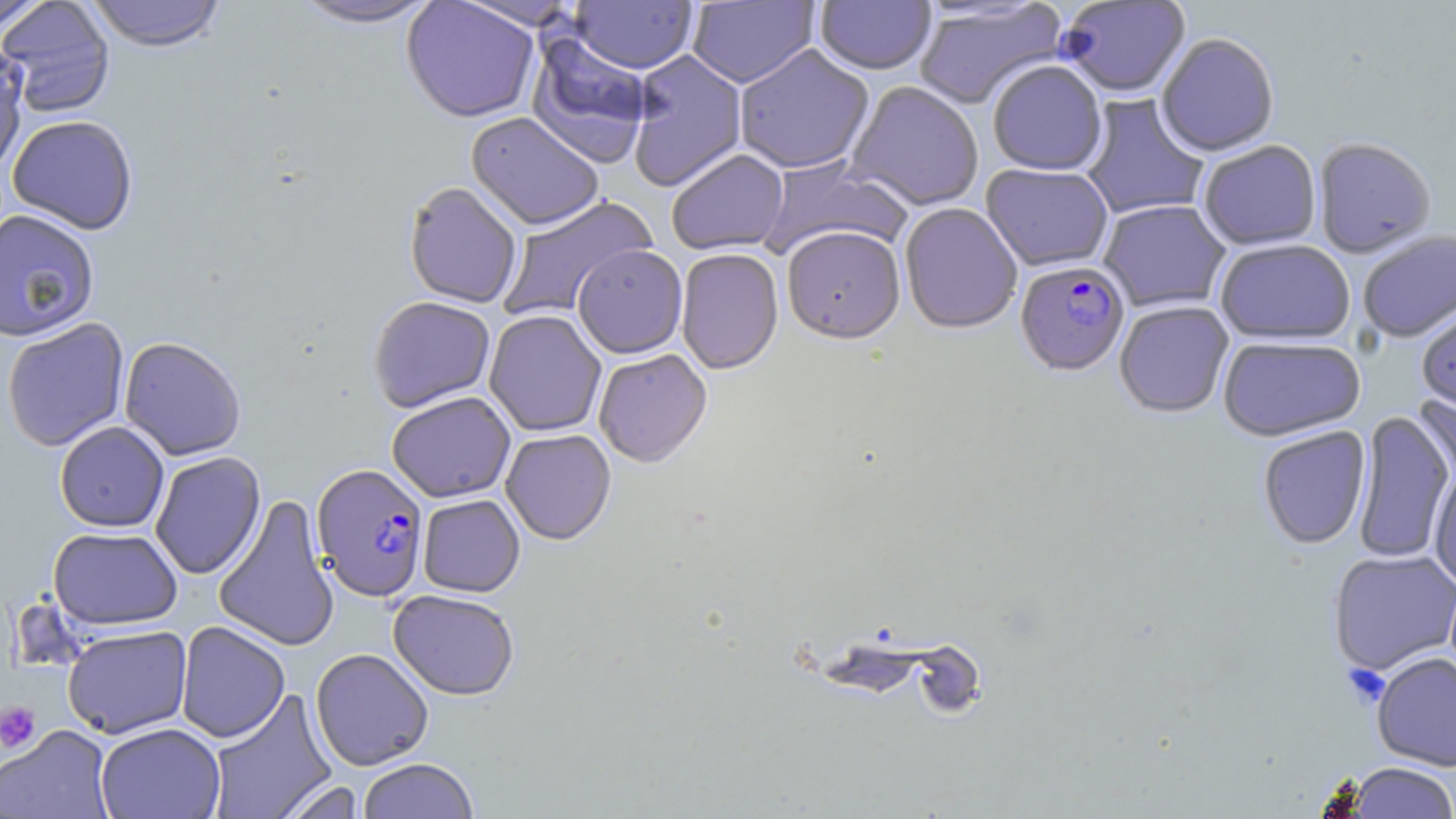
slide-level diagnosis = Plasmodium falciparum
preparation = thin blood smear
uninfected red blood cell locations = approximate bounding boxes as named x1/y1/x2/y2 corners in pixels: (x1=84, y1=0, x2=228, y2=52), (x1=288, y1=0, x2=444, y2=30), (x1=401, y1=0, x2=540, y2=123), (x1=0, y1=1, x2=49, y2=37), (x1=0, y1=1, x2=115, y2=117), (x1=456, y1=1, x2=581, y2=30), (x1=569, y1=1, x2=698, y2=74), (x1=687, y1=1, x2=819, y2=88), (x1=815, y1=1, x2=936, y2=76), (x1=1057, y1=1, x2=1192, y2=99), (x1=913, y1=2, x2=1067, y2=111), (x1=526, y1=29, x2=653, y2=167), (x1=1156, y1=34, x2=1280, y2=159), (x1=0, y1=37, x2=30, y2=175), (x1=734, y1=44, x2=875, y2=174), (x1=627, y1=50, x2=748, y2=192), (x1=987, y1=60, x2=1107, y2=176), (x1=845, y1=81, x2=984, y2=210), (x1=1079, y1=94, x2=1210, y2=220), (x1=466, y1=112, x2=604, y2=230), (x1=7, y1=115, x2=138, y2=234), (x1=1313, y1=138, x2=1436, y2=259), (x1=1199, y1=141, x2=1321, y2=251), (x1=666, y1=149, x2=788, y2=255), (x1=760, y1=156, x2=910, y2=262), (x1=981, y1=164, x2=1114, y2=272), (x1=403, y1=181, x2=523, y2=309), (x1=496, y1=196, x2=657, y2=321), (x1=1098, y1=200, x2=1230, y2=313), (x1=899, y1=203, x2=1022, y2=335), (x1=0, y1=209, x2=100, y2=342), (x1=781, y1=227, x2=906, y2=345), (x1=1358, y1=231, x2=1456, y2=343), (x1=1215, y1=240, x2=1355, y2=345), (x1=572, y1=244, x2=688, y2=359), (x1=676, y1=248, x2=784, y2=375), (x1=368, y1=295, x2=496, y2=412), (x1=1114, y1=301, x2=1234, y2=418), (x1=1416, y1=304, x2=1456, y2=413), (x1=484, y1=310, x2=607, y2=436), (x1=1, y1=318, x2=130, y2=452), (x1=119, y1=335, x2=247, y2=461), (x1=1217, y1=336, x2=1366, y2=442), (x1=594, y1=349, x2=712, y2=468), (x1=386, y1=391, x2=516, y2=503), (x1=1414, y1=393, x2=1455, y2=492), (x1=1352, y1=409, x2=1454, y2=565), (x1=55, y1=421, x2=169, y2=532), (x1=1257, y1=425, x2=1371, y2=550), (x1=501, y1=429, x2=616, y2=545), (x1=150, y1=451, x2=266, y2=579), (x1=1429, y1=464, x2=1456, y2=590), (x1=213, y1=494, x2=339, y2=652), (x1=417, y1=494, x2=525, y2=597), (x1=47, y1=526, x2=183, y2=630), (x1=1328, y1=550, x2=1456, y2=675), (x1=388, y1=589, x2=519, y2=701), (x1=175, y1=621, x2=290, y2=743), (x1=62, y1=625, x2=193, y2=739), (x1=310, y1=647, x2=434, y2=770), (x1=1371, y1=652, x2=1456, y2=772), (x1=207, y1=689, x2=338, y2=819), (x1=95, y1=722, x2=226, y2=819), (x1=1, y1=725, x2=114, y2=819), (x1=356, y1=758, x2=479, y2=819), (x1=1344, y1=763, x2=1456, y2=818), (x1=276, y1=779, x2=366, y2=819)
image size = 1456×819 pixels
stain = May-Grünwald-Giemsa
Plasmodium falciparum-infected red blood cell locations = approximate bounding boxes as named x1/y1/x2/y2 corners in pixels: (x1=1014, y1=260, x2=1131, y2=378), (x1=312, y1=463, x2=429, y2=602)
platelet locations = approximate bounding boxes as named x1/y1/x2/y2 corners in pixels: (x1=0, y1=701, x2=41, y2=754)
modality = optical microscopy
magnification = 1000x
field of view = one of a larger specimen